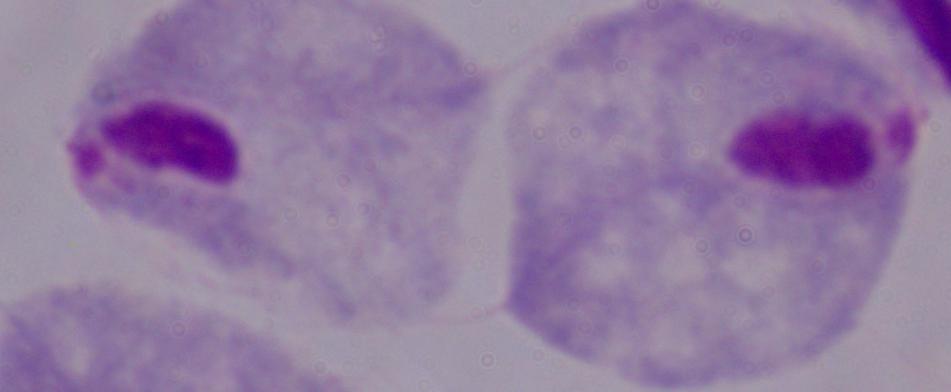
magnification = 1000x
identification = trichomonad
modality = photomicrograph